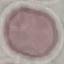
Summary:
  - Malaria status: uninfected
  - Capture: smartphone camera at the microscope eyepiece
  - Image type: automatically extracted cell patch, resized to 64 × 64 pixels
  - Preparation: thin blood film
  - Stain: Giemsa